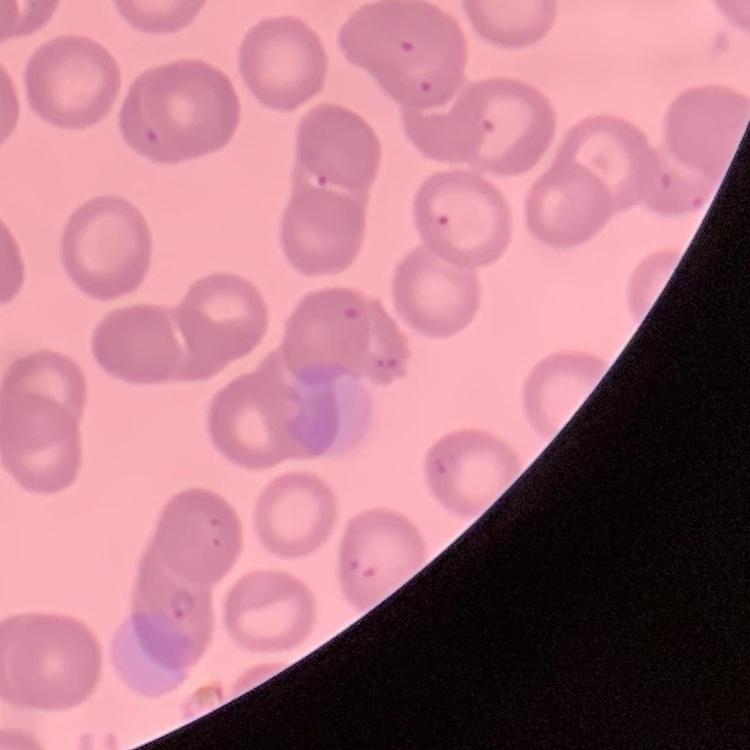
Summary:
  - Red blood cell morphology: no rouleaux formation
  - Preparation: thin blood smear
  - Image type: one tile cut from a larger photomicrograph
  - Stain: Field's or Giemsa